Comment on the morphology of the erythrocytes.
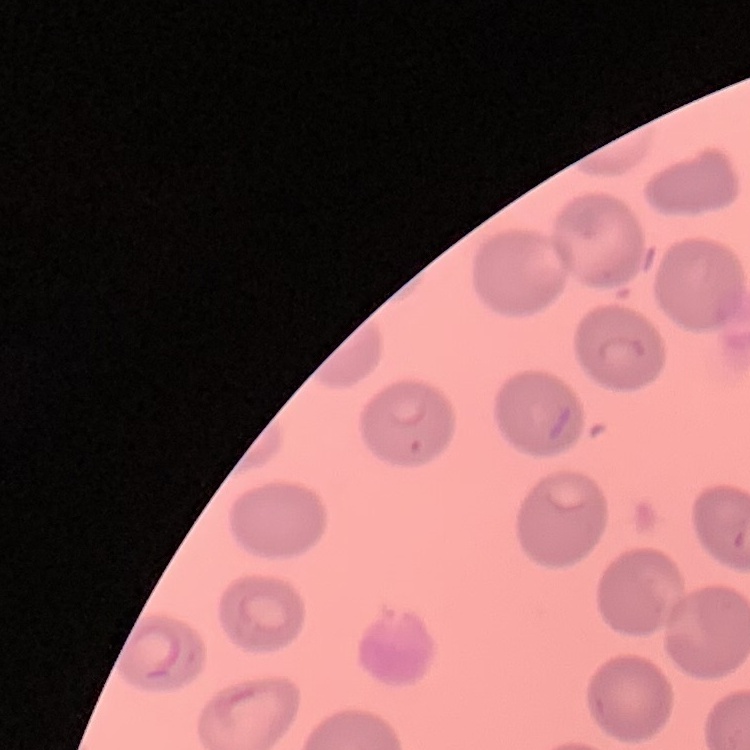

No rouleaux formation.

Field's or Giemsa stain. Thin blood smear. Square crop of a larger photomicrograph.